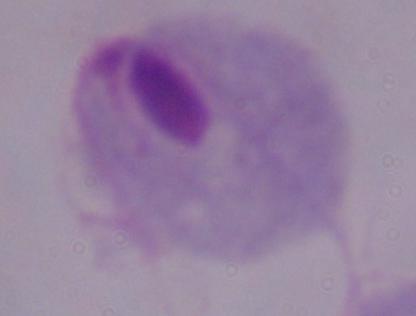
magnification: 1000x
identification: trichomonad
modality: photomicrograph